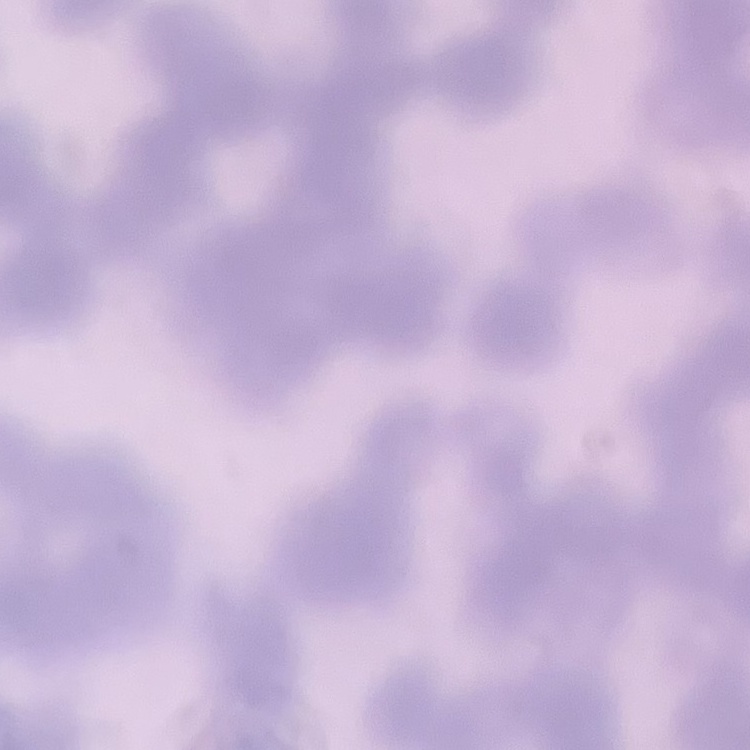

erythrocyte_morphology: rouleaux formation
stain: Field's or Giemsa
preparation: thin blood smear
image_type: square crop of a larger photomicrograph